Report the malaria status of this cell.
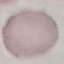
It is uninfected.

preparation: thin blood smear
capture: smartphone camera at the microscope eyepiece
stain: Giemsa
image_type: automatically extracted cell patch, resized to 64 × 64 pixels